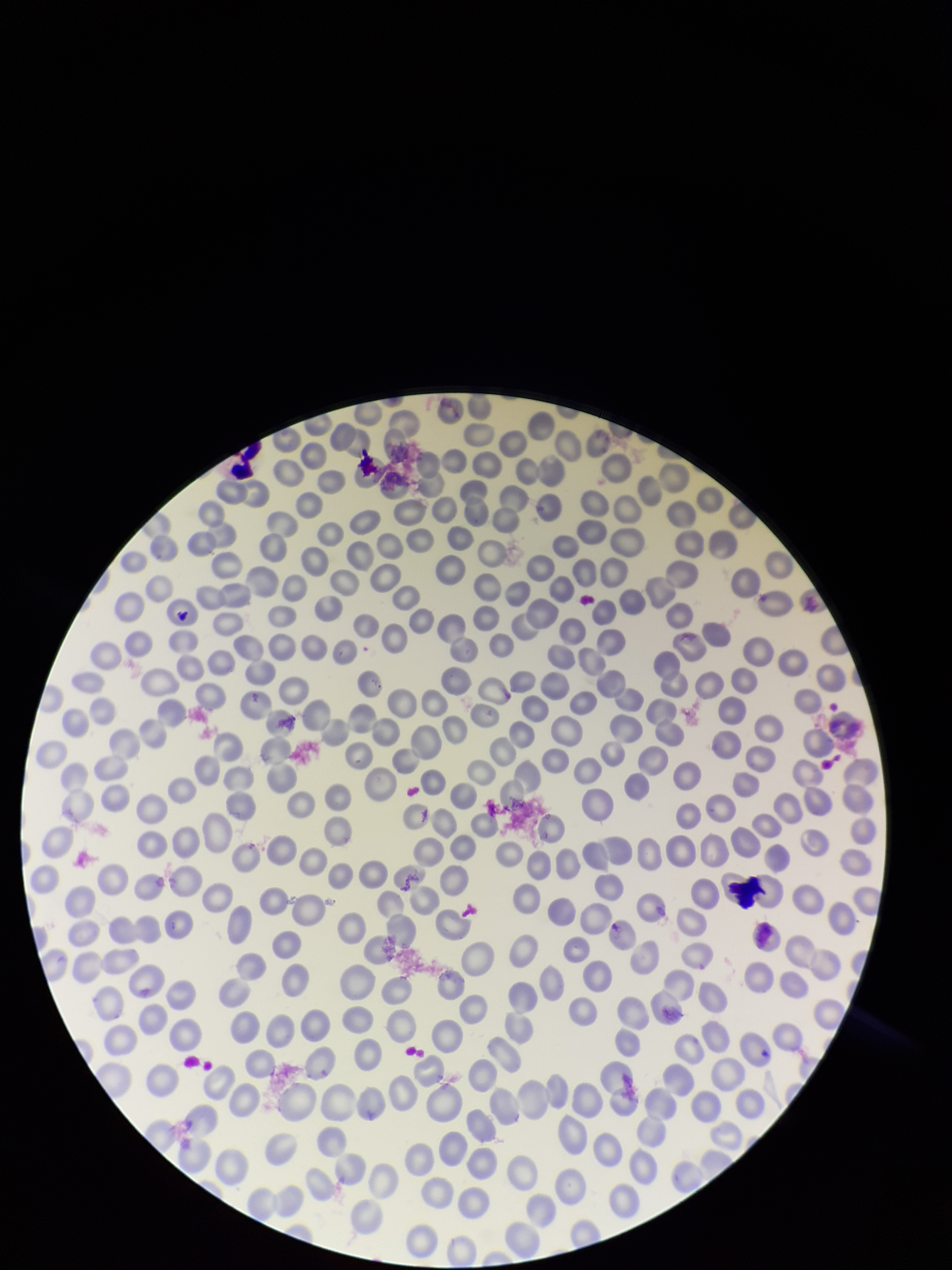

Red blood cell count: 303. Preparation: thin. Stained with Giemsa. Photographed through the microscope eyepiece with a smartphone camera. Image is 952×1270 pixels. Patient malaria status: negative. Parasitized red blood cells: none detected. Single field of view. Parasitized red blood cell count: 0.